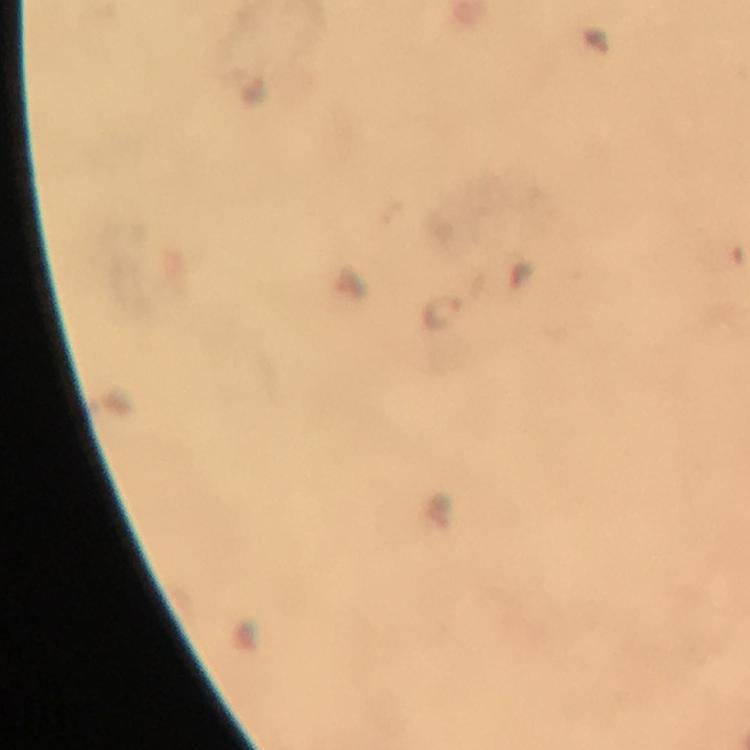

Approximate object centers, in pixels from the top-left corner. Plasmodium parasite locations: (x=442, y=317). From a diagnostic examination for malaria. Photographed with a smartphone mounted on the microscope. At 100x magnification. Cropped region of a single field of view. Image is 750×750 pixels. Giemsa-stained preparation. Thick blood smear. Immersion oil was used.